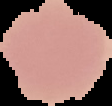
malaria status = uninfected
image type = segmented cell region with the area outside set to black
image size = 112×106 pixels
preparation = thin blood smear